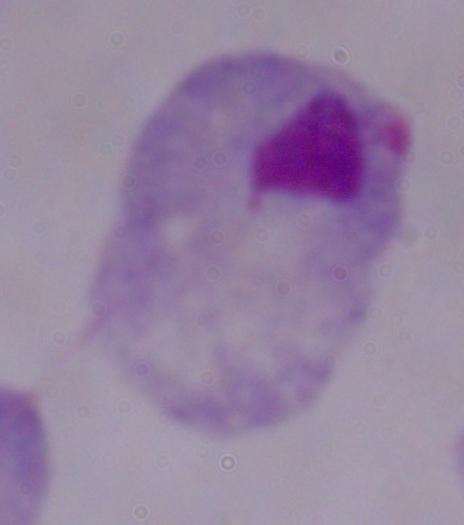

Summary:
  - Modality: micrograph
  - Identification: trichomonad
  - Magnification: 1000x